Give the position of every Plasmodium parasite visible.
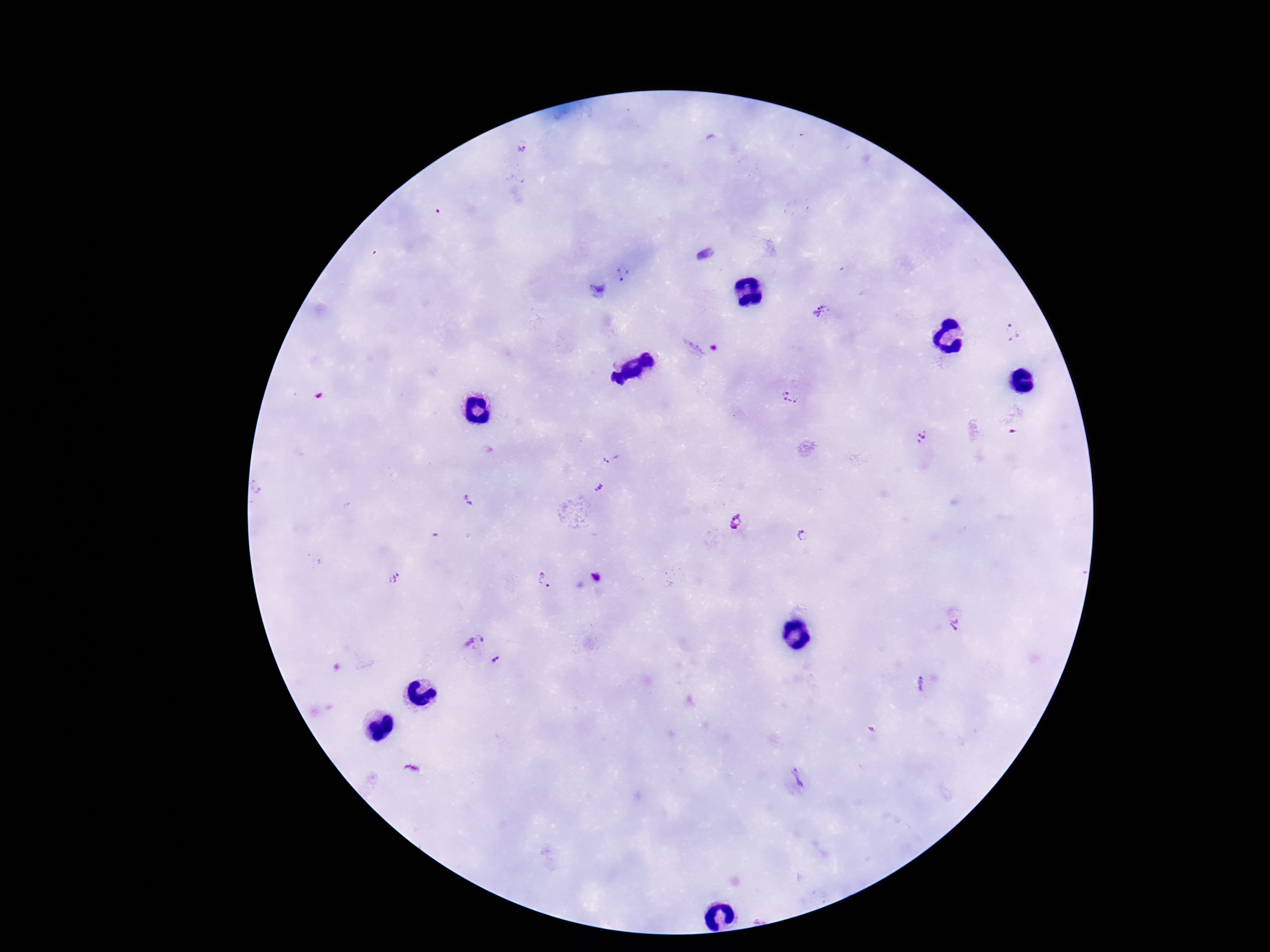

Approximate object centers, in pixels from the top-left corner.
Plasmodium parasites: (x=522, y=148), (x=703, y=253), (x=622, y=275), (x=597, y=290), (x=822, y=311), (x=1011, y=332), (x=702, y=345), (x=791, y=398), (x=1015, y=420), (x=922, y=437), (x=611, y=458), (x=600, y=487), (x=468, y=500), (x=735, y=521), (x=802, y=536), (x=393, y=577), (x=596, y=578), (x=545, y=581), (x=955, y=623), (x=473, y=640), (x=496, y=661), (x=920, y=685), (x=797, y=778).

Summary:
  - Magnification: 100x
  - Capture: smartphone camera through the microscope eyepiece
  - Stain: Giemsa
  - Preparation: thick blood film
  - Image size: 1270×952 pixels
  - Patient malaria status: infected
  - Field of view: one from this slide